Name the parasite shown.
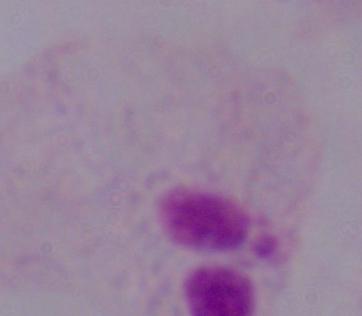
A trichomonad.

magnification = 1000x
modality = micrograph